Comment on the morphology of the red blood cells.
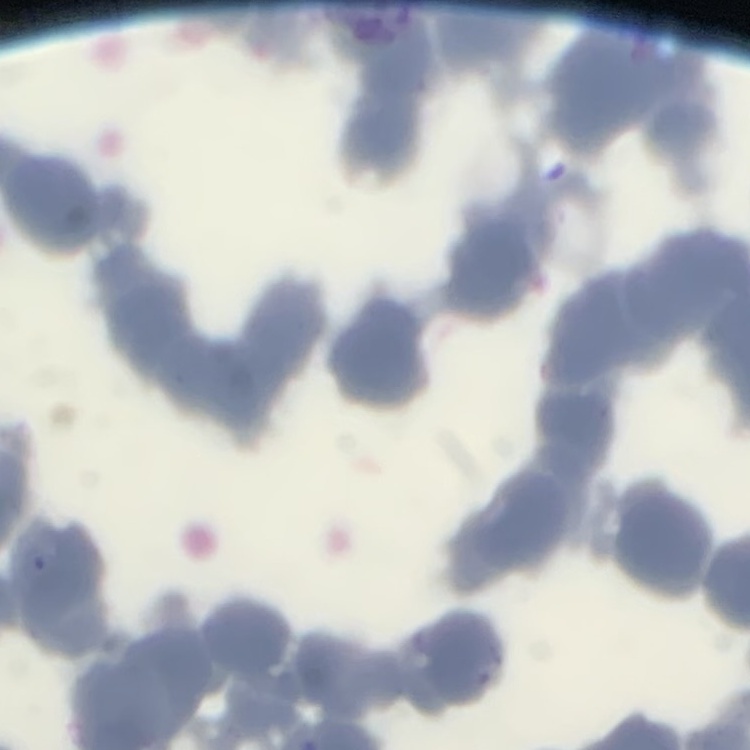
Rouleaux formation.

Summary:
  - Stain: Field's or Giemsa
  - Image type: one tile cut from a larger photomicrograph
  - Preparation: thin peripheral smear